Comment on the morphology of the red blood cells.
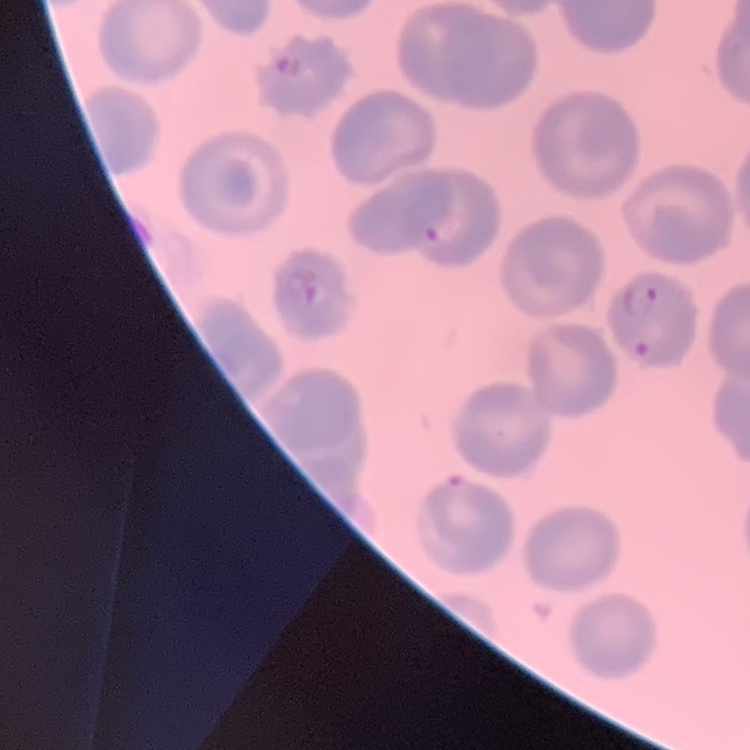
No rouleaux formation.

preparation: thin peripheral smear
image_type: square crop of a larger photomicrograph
stain: Field's or Giemsa